Assess the morphology of the erythrocytes.
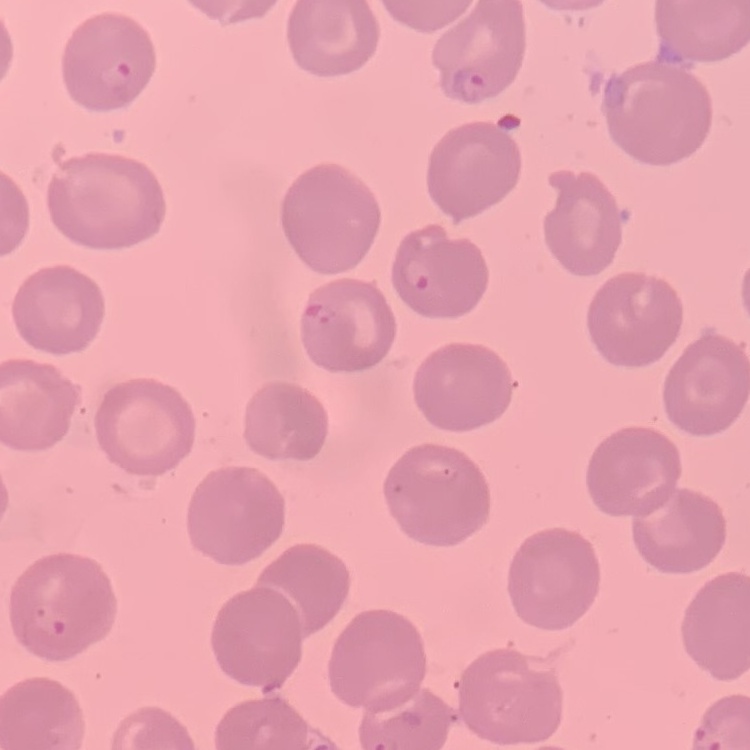

They show no rouleaux formation.

One tile cut from a larger photomicrograph. Field's or Giemsa stain. Thin blood smear.